Locate every Plasmodium parasite.
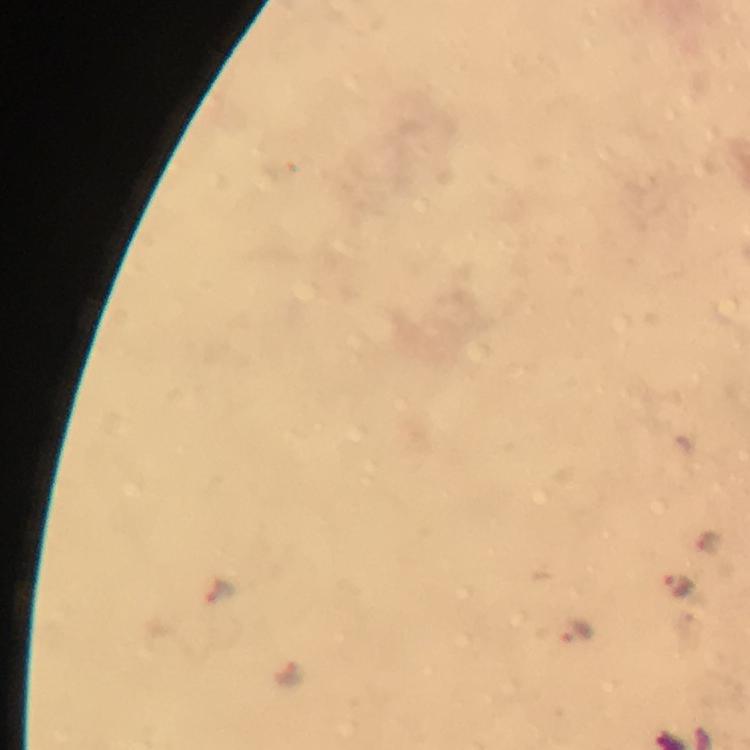
Approximate centers as (x, y) in pixels.
Plasmodium parasites: (682, 586), (578, 629), (291, 671).

Summary:
  - Immersion oil: applied
  - Context: from a diagnostic examination for malaria
  - Capture: smartphone photograph through a microscope
  - Magnification: 100x
  - Stain: Giemsa
  - Image size: 750×750 pixels
  - Cropped from: a single field of view
  - Preparation: thick blood smear